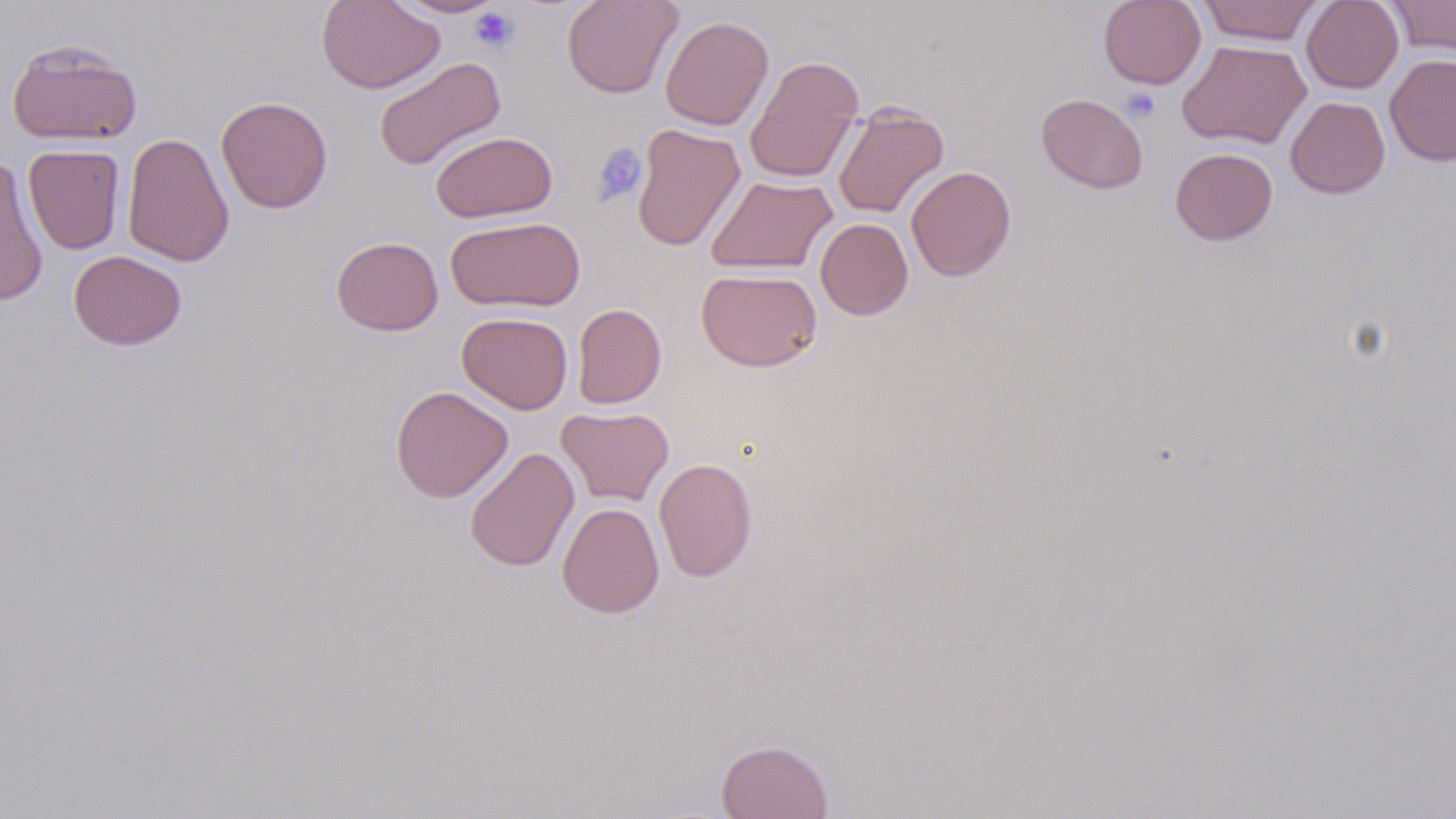 Approximate bounding boxes as (x1,y1)-(x2,y2) corner pairs in pixels. Uninfected red blood cell locations: (317,0)-(444,94), (388,0)-(508,18), (561,0)-(682,99), (1098,0)-(1206,89), (1197,0)-(1324,46), (1301,0)-(1404,94), (1386,0)-(1456,59), (660,15)-(774,131), (6,38)-(143,147), (1177,40)-(1311,150), (1384,54)-(1456,166), (745,55)-(864,183), (374,56)-(506,171), (1036,93)-(1148,194), (216,96)-(333,213), (1285,96)-(1390,198), (832,104)-(949,218), (631,123)-(745,251), (430,130)-(557,223), (121,132)-(234,267), (23,144)-(125,254), (1170,147)-(1278,246), (0,159)-(48,307), (906,165)-(1016,281), (705,175)-(838,275), (446,216)-(585,313), (815,218)-(913,320), (331,236)-(444,336), (68,250)-(187,351), (696,268)-(822,372), (572,303)-(666,409), (456,312)-(573,414), (391,386)-(513,503), (556,406)-(674,506), (464,447)-(580,572), (653,458)-(757,582), (557,502)-(664,618), (716,739)-(833,818). Platelet locations: (469,7)-(519,52), (1121,87)-(1161,122), (591,142)-(648,205). Slide-level diagnosis: no evidence of blood parasites. May-Grünwald-Giemsa stain. 1000x magnification. One field of a larger specimen. Image is 1456×819 pixels. Thin blood smear. Optical microscopy.